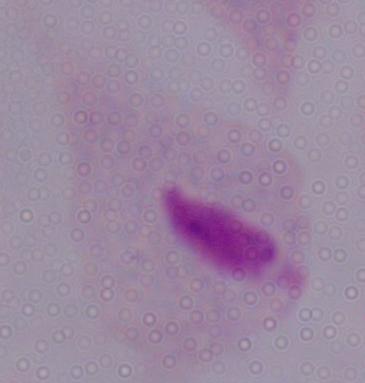 1000x magnification. Photomicrograph. A trichomonad is seen.